Comment on the morphology of the red blood cells.
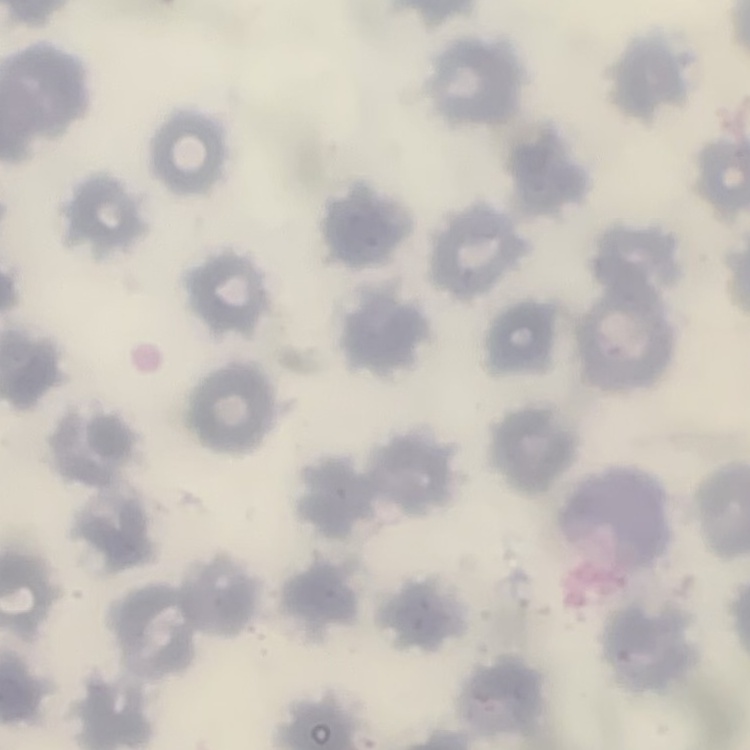
No rouleaux formation.

image type = square crop of a larger photomicrograph
stain = Field's or Giemsa
preparation = thin blood smear